Identify the parasite.
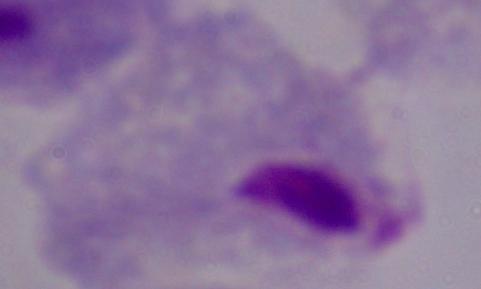
A trichomonad.

Summary:
  - Magnification: 1000x
  - Modality: micrograph